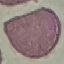
Malaria status: uninfected. Giemsa-stained preparation. Thin blood film. Cell patch, automatically extracted from a larger field of view and resized to 64 × 64 pixels. Acquired by smartphone through the microscope eyepiece.